Locate every Plasmodium parasite and identify its life-cycle stage.
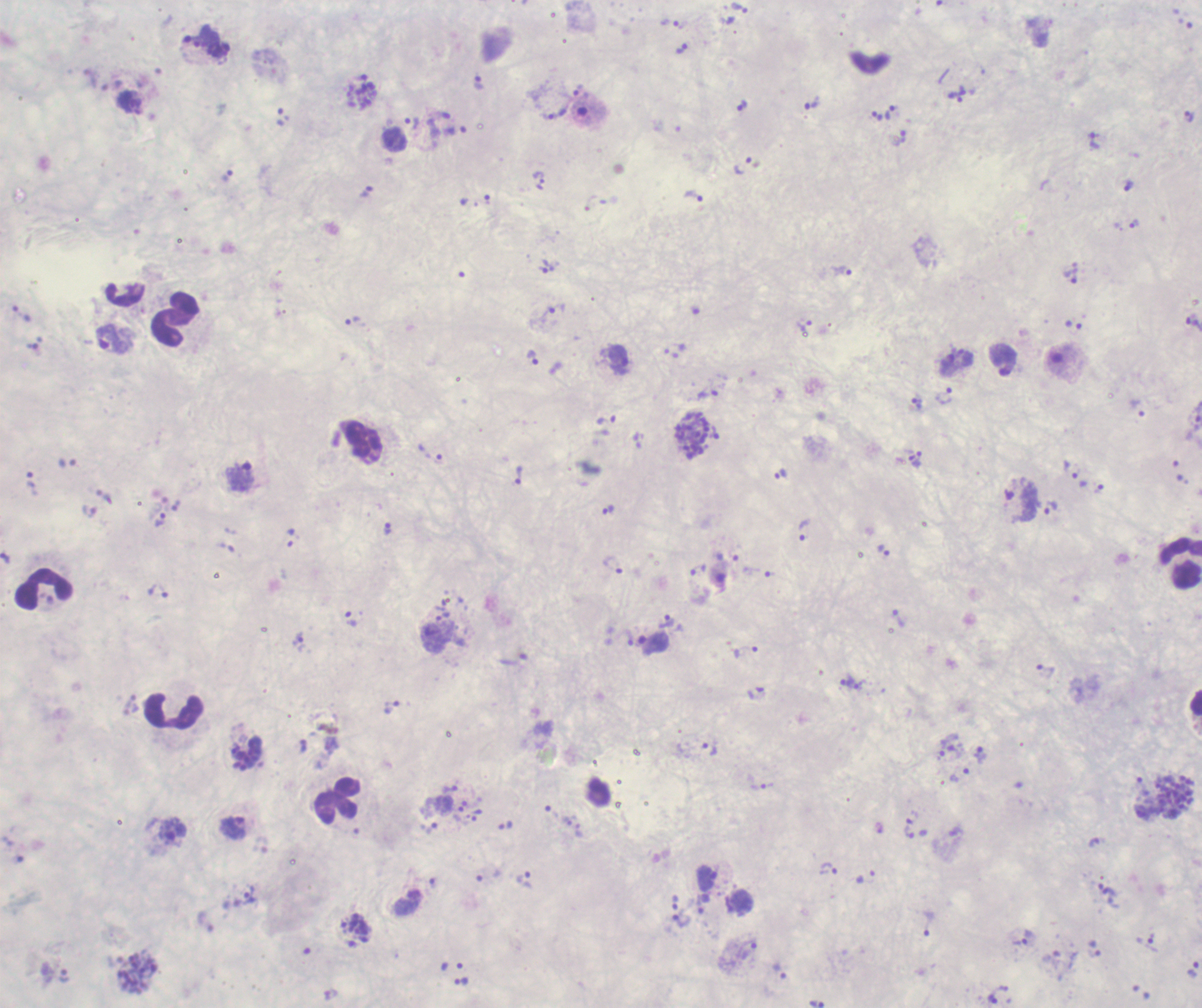
Approximate centers as {x, y} in pixels.
Trophozoites: {739, 8}, {670, 23}, {681, 48}, {479, 82}, {957, 95}, {811, 105}, {742, 106}, {889, 112}, {558, 114}, {877, 115}, {1189, 117}, {412, 122}, {1095, 141}, {743, 165}, {539, 179}, {366, 192}, {694, 195}, {1134, 224}, {547, 267}, {843, 271}, {1070, 276}, {22, 314}, {352, 321}, {806, 326}, {113, 339}, {533, 357}, {1003, 360}, {708, 394}, {944, 396}, {607, 421}, {692, 436}, {430, 454}, {915, 462}, {781, 473}, {519, 474}, {241, 476}, {1080, 480}, {32, 483}, {1020, 503}, {177, 505}, {1051, 509}, {608, 510}, {89, 511}, {160, 519}, {388, 529}, {803, 529}, {884, 550}, {614, 565}, {158, 591}, {442, 616}, {899, 618}, {352, 620}, {667, 620}, {300, 641}, {653, 642}, {1045, 672}, {847, 680}, {860, 685}, {757, 694}, {392, 706}, {949, 742}, {710, 749}, {238, 751}, {981, 755}, {959, 774}, {761, 782}, {451, 788}, {552, 813}, {429, 828}, {234, 829}, {580, 830}, {173, 832}, {910, 832}, {828, 869}, {866, 876}, {709, 878}, {524, 879}, {1107, 890}, {250, 894}, {703, 903}, {682, 920}, {929, 924}, {1022, 938}, {1147, 942}, {1193, 969}, {462, 982}, {993, 999}.
Schizonts: {362, 92}, {1165, 798}, {138, 972}.
No gametocyte forms observed.

Approximate centers as {x, y} in pixels.
Summary:
  - Leukocyte locations: {175, 319}, {1180, 562}, {43, 589}, {173, 709}, {338, 801}
  - Coloration quality: bad
  - Magnification: 100x
  - Field of view: single
  - Image size: 1202×1008 pixels
  - Stain: Romanowsky
  - Preparation: thick smear of blood
  - Background quality: poor
  - Context: previously used in an actual diagnosis